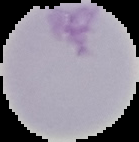

Image is 139×142 pixels. Segmented cell region on a black background. Result: no malaria parasites detected. From a thin blood film.